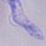
magnification = 1000x
identification = trypanosome
modality = photomicrograph